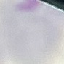
Summary:
  - Result: no malaria parasites detected
  - Stain: Giemsa
  - Capture: smartphone camera at the microscope eyepiece
  - Preparation: thin smear
  - Image type: cell patch, automatically extracted from a larger field of view and resized to 64 × 64 pixels